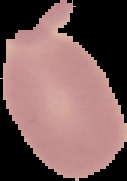

image_size: 127×181 pixels
preparation: thin blood film
result: no malaria parasites seen
image_type: cell region segmented out of the field of view; surrounding area masked to black